Assess the morphology of the erythrocytes.
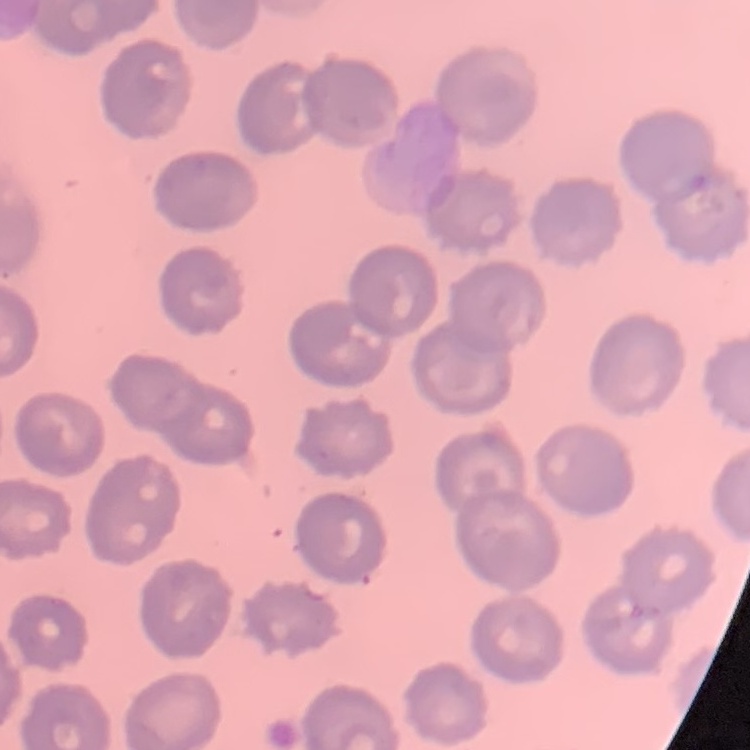
They show no rouleaux formation.

Summary:
  - Preparation: thin blood smear
  - Stain: Field's or Giemsa
  - Image type: one tile cut from a larger photomicrograph